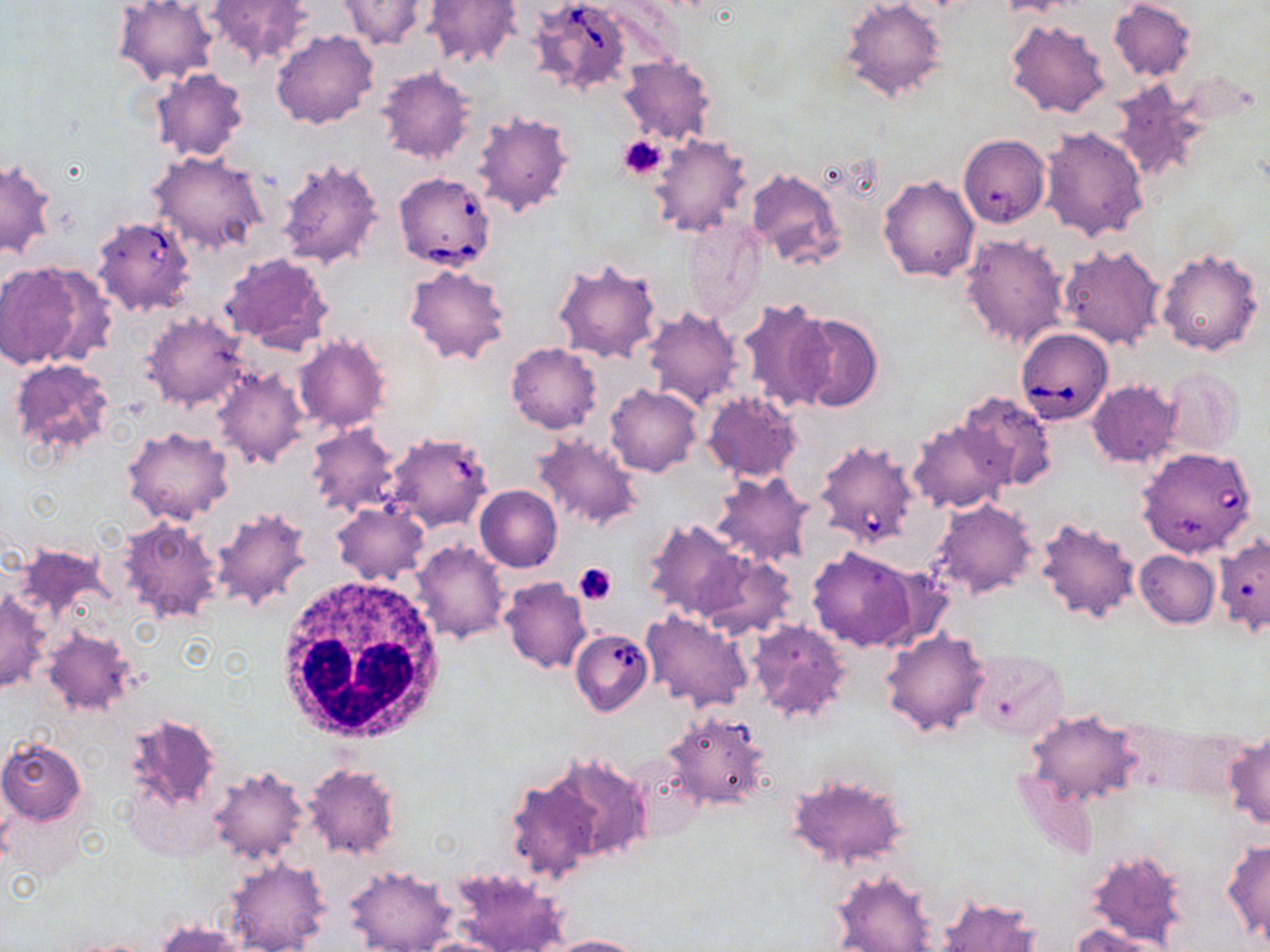
Approximate bounding boxes as [x1, y1, x2, y2] in pixels. White blood cell locations: [272, 578, 447, 744]. Platelet locations: [617, 135, 668, 179], [573, 562, 617, 606]. Uninfected red blood cell locations: [204, 0, 314, 70], [336, 0, 431, 50], [423, 0, 522, 69], [839, 0, 949, 104], [1109, 0, 1196, 80], [114, 1, 219, 85], [1006, 18, 1111, 119], [271, 29, 378, 130], [617, 55, 715, 146], [375, 67, 475, 165], [150, 68, 250, 162], [1107, 78, 1207, 184], [472, 112, 574, 218], [1039, 126, 1148, 241], [647, 133, 752, 238], [958, 133, 1050, 228], [149, 149, 268, 256], [274, 154, 384, 271], [2, 157, 56, 260], [745, 166, 847, 271], [878, 173, 980, 282], [680, 214, 767, 323], [959, 233, 1071, 353], [1059, 243, 1165, 351], [1157, 246, 1264, 356], [220, 253, 334, 353], [552, 256, 663, 365], [0, 260, 102, 369], [404, 264, 509, 365], [736, 298, 835, 412], [642, 305, 742, 410], [143, 310, 249, 412], [786, 311, 882, 412], [294, 336, 390, 433], [506, 343, 601, 433], [9, 359, 116, 462], [1161, 366, 1246, 458], [212, 367, 310, 469], [1087, 379, 1182, 470], [605, 385, 701, 477], [960, 391, 1056, 490], [702, 392, 803, 482], [908, 418, 1014, 514], [305, 423, 401, 517], [122, 426, 234, 526], [530, 433, 643, 532], [709, 471, 815, 567], [474, 485, 562, 572], [929, 498, 1038, 601], [331, 500, 429, 585], [210, 506, 313, 612], [118, 515, 225, 624], [1034, 516, 1142, 625], [643, 519, 749, 621], [411, 541, 510, 643], [13, 543, 115, 625], [807, 546, 919, 651], [1134, 549, 1220, 628], [698, 554, 796, 641], [500, 577, 591, 674], [0, 592, 51, 693], [639, 610, 751, 712], [747, 619, 854, 727], [41, 626, 139, 715], [881, 627, 992, 739], [969, 650, 1068, 741], [123, 710, 224, 839], [662, 710, 771, 811], [1024, 710, 1142, 806], [1224, 734, 1270, 831], [0, 738, 86, 825], [545, 750, 656, 863], [302, 763, 401, 860], [208, 766, 309, 864], [783, 774, 910, 869], [504, 776, 603, 887], [1222, 839, 1270, 948], [1084, 845, 1190, 952], [223, 855, 331, 952], [344, 865, 457, 951], [449, 866, 567, 952], [831, 870, 938, 951], [936, 895, 1042, 952], [154, 920, 246, 951], [1072, 923, 1170, 952], [539, 934, 650, 951]. Babesia divergens-infected red blood cell locations: [529, 0, 632, 96], [393, 172, 496, 270], [91, 213, 196, 317], [1015, 328, 1114, 426], [393, 439, 488, 532], [814, 439, 921, 549], [1137, 447, 1259, 558], [570, 628, 654, 716]. Slide-level diagnosis: Babesia divergens. Single field of view. May-Grünwald-Giemsa-stained preparation. Thin blood film. Optical microscopy. Captured at 1000x magnification. Image is 1270×952 pixels.